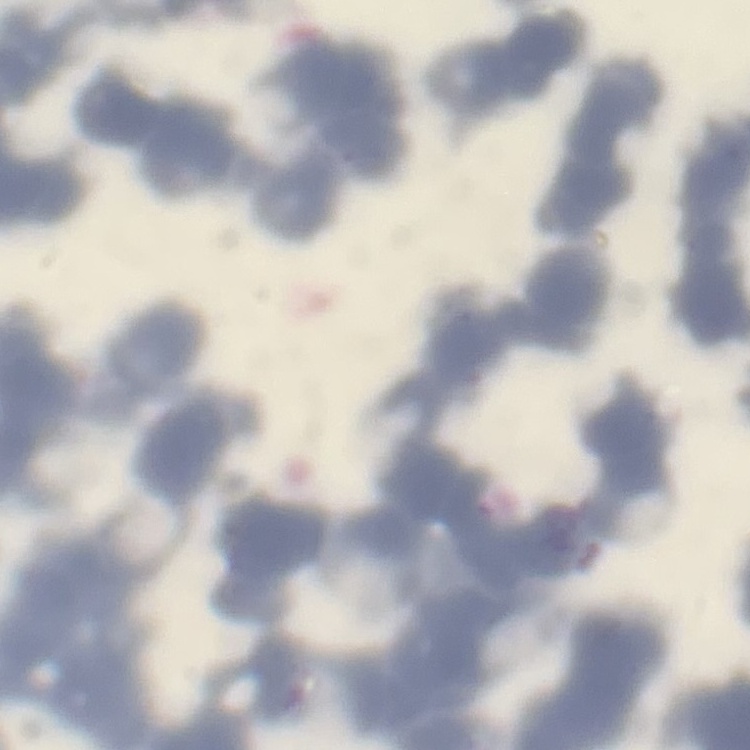
{
  "erythrocyte_morphology": "rouleaux formation",
  "image_type": "one tile cut from a larger photomicrograph",
  "preparation": "thin blood smear",
  "stain": "Field's or Giemsa"
}